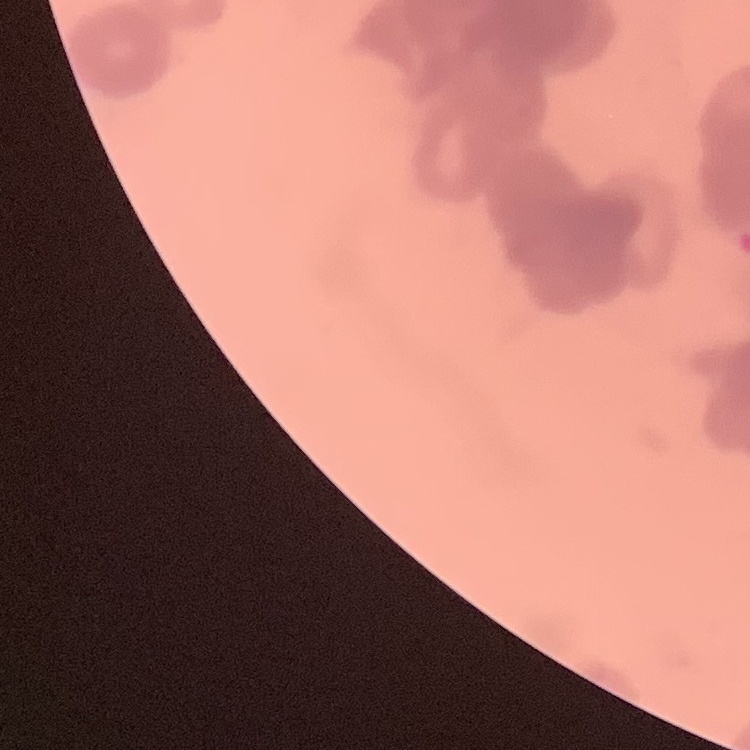
Summary:
  - Red blood cell morphology: rouleaux formation
  - Preparation: thin blood smear
  - Stain: Field's or Giemsa
  - Image type: square crop of a larger photomicrograph